Locate every malaria parasite.
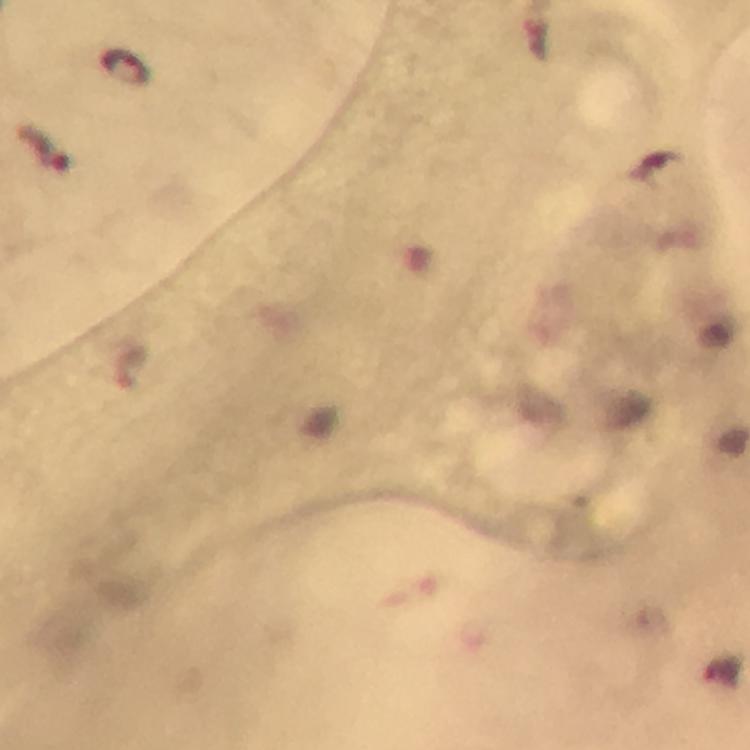
Approximate centers as {x, y} in pixels.
Malaria parasites: {124, 66}.

From a diagnostic examination for malaria. Cropped region of a single field of view. Smartphone photograph taken through a microscope. Thick smear. Giemsa-stained preparation. Image is 750×750 pixels. 100x magnification. Immersion oil applied.